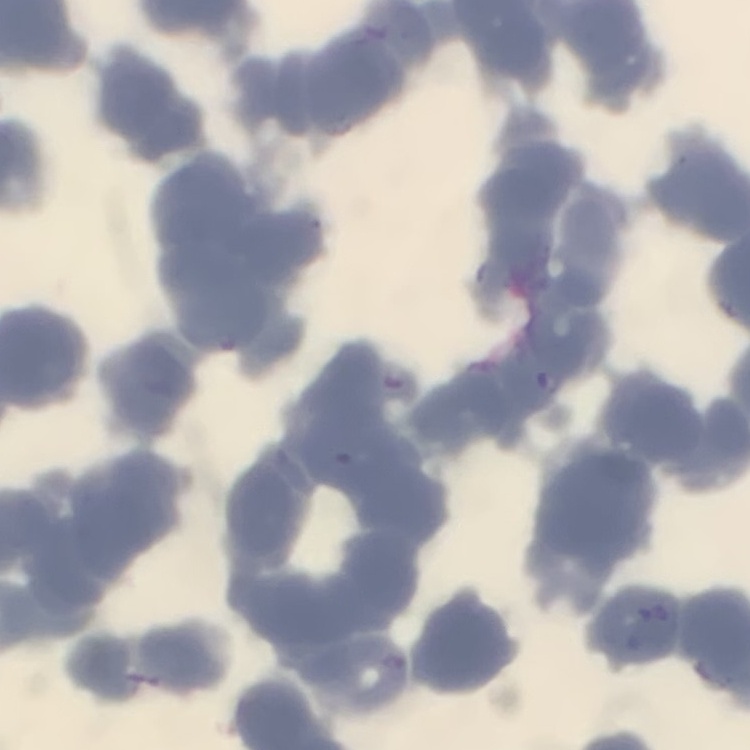

erythrocyte morphology = rouleaux formation
image type = one tile cut from a larger photomicrograph
stain = Field's or Giemsa
preparation = thin blood film